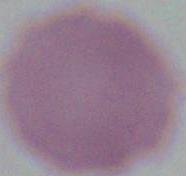
1000x magnification. Micrograph. An erythrocyte is shown.